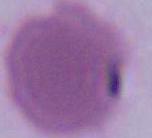

Summary:
  - Modality: photomicrograph
  - Identification: red blood cell
  - Magnification: 1000x